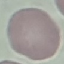
Malaria status: uninfected. Automatically extracted cell patch, resized to 64 × 64 pixels. Acquired by smartphone through the microscope eyepiece. Giemsa stain. Thin blood smear.